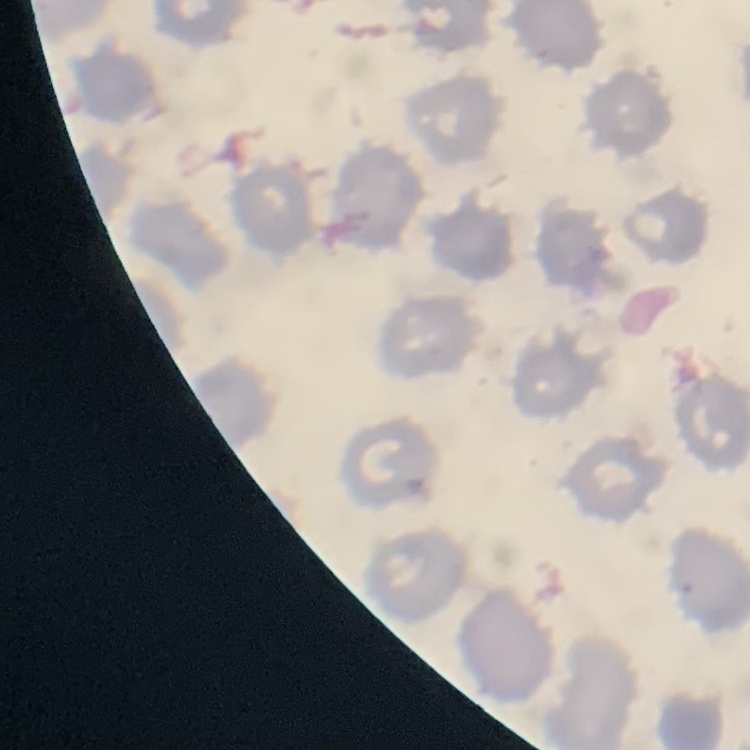

The red blood cells show no rouleaux formation. One tile cut from a larger photomicrograph. Thin blood smear. Field's or Giemsa stain.